Classify this cell by malaria status.
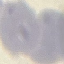
It is uninfected.

stain = Giemsa
capture = smartphone through the microscope eyepiece
preparation = thin smear
image type = cell patch, automatically extracted from a larger field of view and resized to 64 × 64 pixels